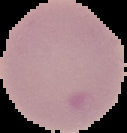
Image is 127×133 pixels. From a thin blood film. Cell region segmented out of the field of view; the surrounding area is masked to black. Result: negative for Plasmodium parasites.